Classify this cell by malaria status.
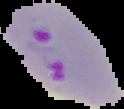

Parasitized.

preparation = thin blood smear
image size = 124×109 pixels
image type = cell region segmented out of the field of view; surrounding area masked to black